Comment on the morphology of the erythrocytes.
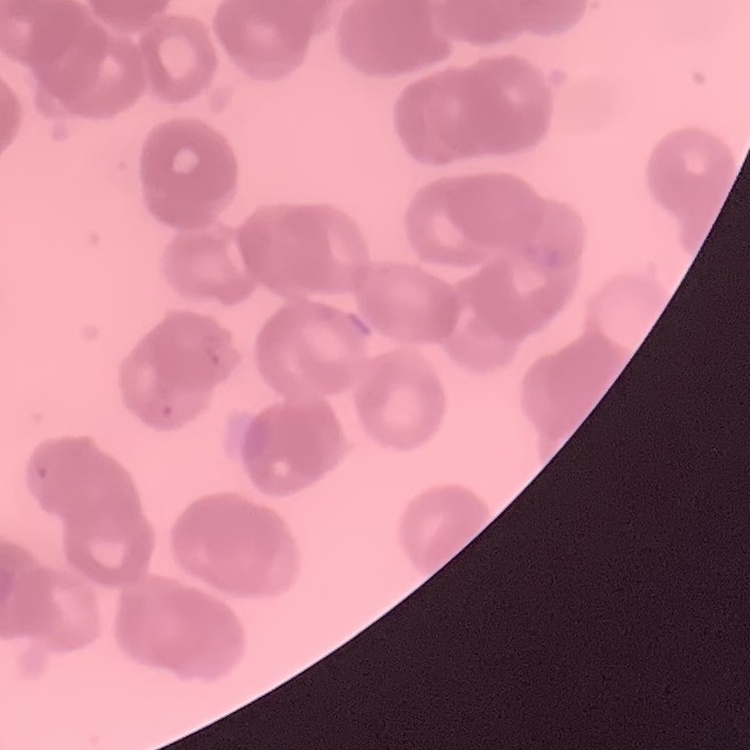
They show rouleaux formation.

stain = Field's or Giemsa
preparation = thin blood smear
image type = square crop of a larger photomicrograph